Name the parasite shown.
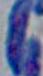
Toxoplasma gondii.

magnification: 1000x
modality: micrograph